Evaluate for Plasmodium parasites.
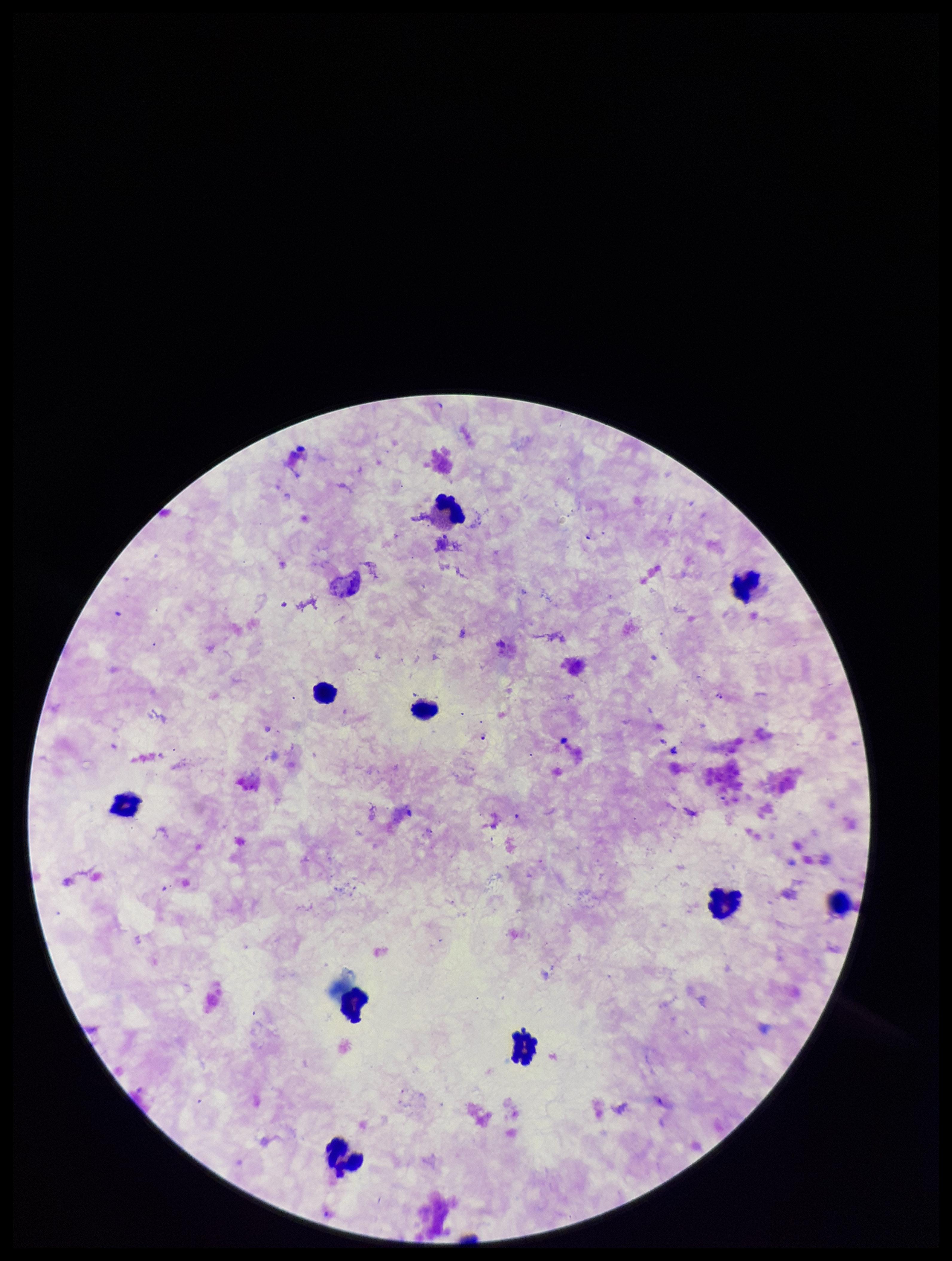
Identified.

Photographed through the microscope eyepiece with a smartphone camera. Image is 952×1261 pixels. Species reported for this patient: Plasmodium falciparum. Patient malaria status: infected. Stained with Giemsa. Parasite count: 2. Leukocyte count: 10. One field from this slide. Preparation: thick blood smear.